Locate and identify every blood parasite.
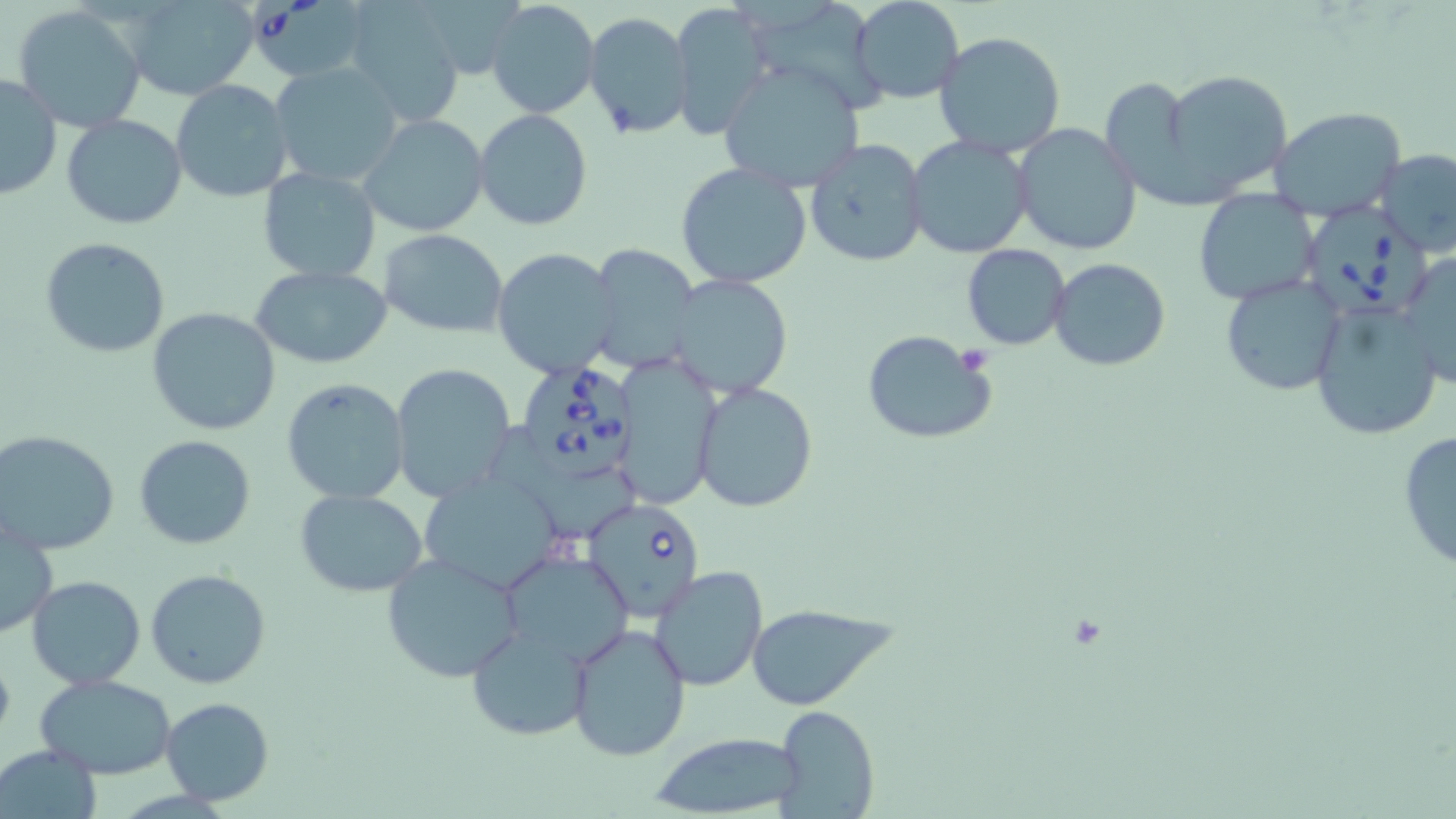

Approximate bounding boxes as [x1, y1, x2, y2] in pixels.
Babesia divergens-infected red blood cells: [253, 0, 361, 74], [1300, 207, 1430, 315], [513, 360, 641, 480], [582, 497, 706, 619].
No Plasmodium falciparum, Plasmodium ovale, Plasmodium malariae, Plasmodium vivax, or Trypanosoma brucei observed.

slide_level_diagnosis: Babesia divergens
modality: optical microscopy
stain: May-Grünwald-Giemsa
image_size: 1456×819 pixels
preparation: thin blood film
platelet_locations: 'approximate bounding boxes as [x1, y1, x2, y2] in pixels: [960, 345, 991, 375]'
magnification: 1000x
uninfected_red_blood_cell_locations: 'approximate bounding boxes as [x1, y1, x2, y2] in pixels: [124, 0, 261, 100], [485, 0, 600, 119], [849, 0, 964, 105], [667, 2, 774, 139], [345, 3, 468, 125], [12, 8, 144, 130], [584, 11, 696, 139], [935, 31, 1067, 158], [269, 62, 404, 190], [718, 63, 864, 192], [1160, 69, 1290, 198], [1, 72, 63, 201], [171, 79, 294, 202], [65, 94, 293, 213], [1269, 105, 1405, 220], [473, 109, 593, 230], [63, 113, 187, 230], [360, 113, 491, 238], [1012, 124, 1141, 256], [906, 136, 1032, 258], [805, 140, 928, 267], [1376, 147, 1456, 255], [676, 163, 811, 289], [257, 167, 382, 281], [1195, 188, 1319, 306], [380, 230, 509, 336], [40, 236, 170, 358], [586, 244, 700, 371], [961, 244, 1070, 349], [493, 248, 620, 378], [1400, 250, 1456, 392], [1048, 257, 1172, 372], [250, 265, 394, 367], [667, 273, 793, 399], [1220, 275, 1348, 396], [1308, 302, 1444, 442], [147, 307, 280, 436], [862, 330, 996, 445], [615, 354, 722, 511], [392, 363, 517, 500], [282, 377, 411, 504], [693, 380, 819, 514], [1396, 428, 1456, 571], [1, 429, 120, 554], [135, 434, 256, 550], [417, 471, 571, 595], [294, 488, 429, 597], [1, 519, 57, 637], [496, 549, 632, 671], [381, 554, 526, 683], [650, 566, 768, 691], [146, 568, 272, 690], [26, 575, 145, 689], [747, 604, 889, 710], [567, 621, 691, 762], [468, 623, 592, 740], [33, 674, 179, 777], [159, 697, 274, 805], [771, 703, 879, 818], [647, 730, 805, 818], [1, 743, 103, 818]'
field_of_view: single